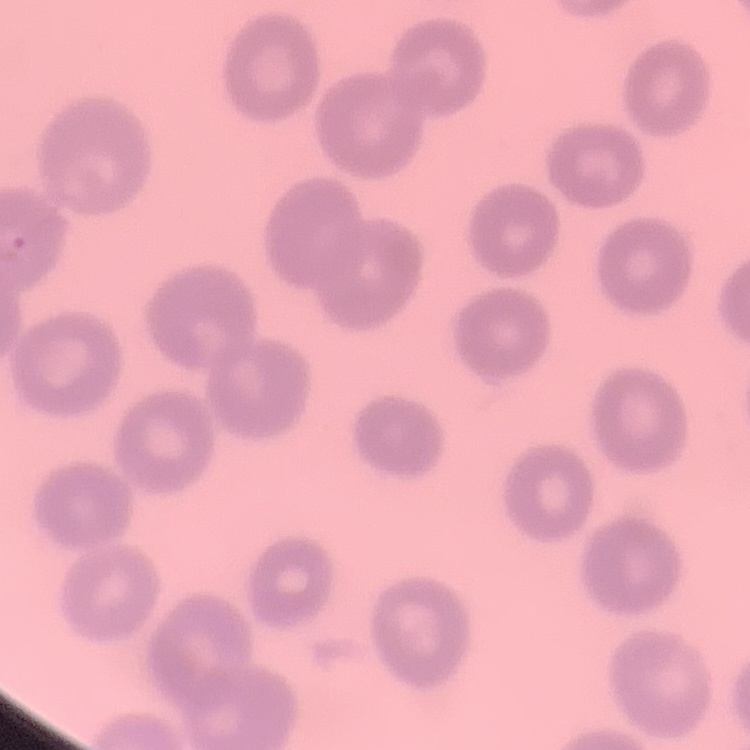
red blood cell morphology = no rouleaux formation
image type = one tile cut from a larger photomicrograph
stain = Field's or Giemsa
preparation = thin blood film